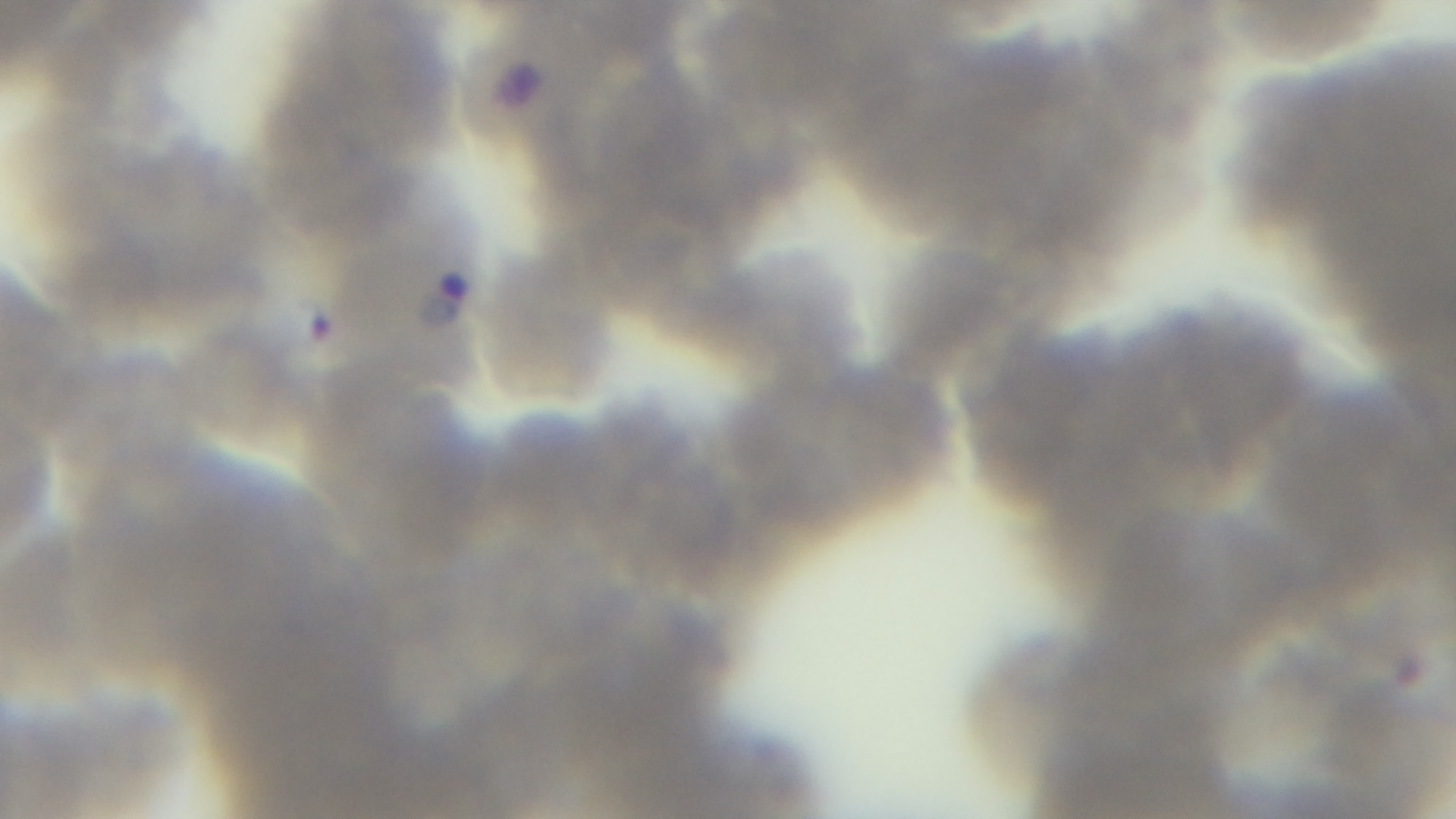

field of view = single
capture = mounted 4K digital camera
objective = 100x oil immersion
modality = light microscopy
stain = Giemsa
preparation = thin blood film
malaria status = infected